Locate every malaria parasite.
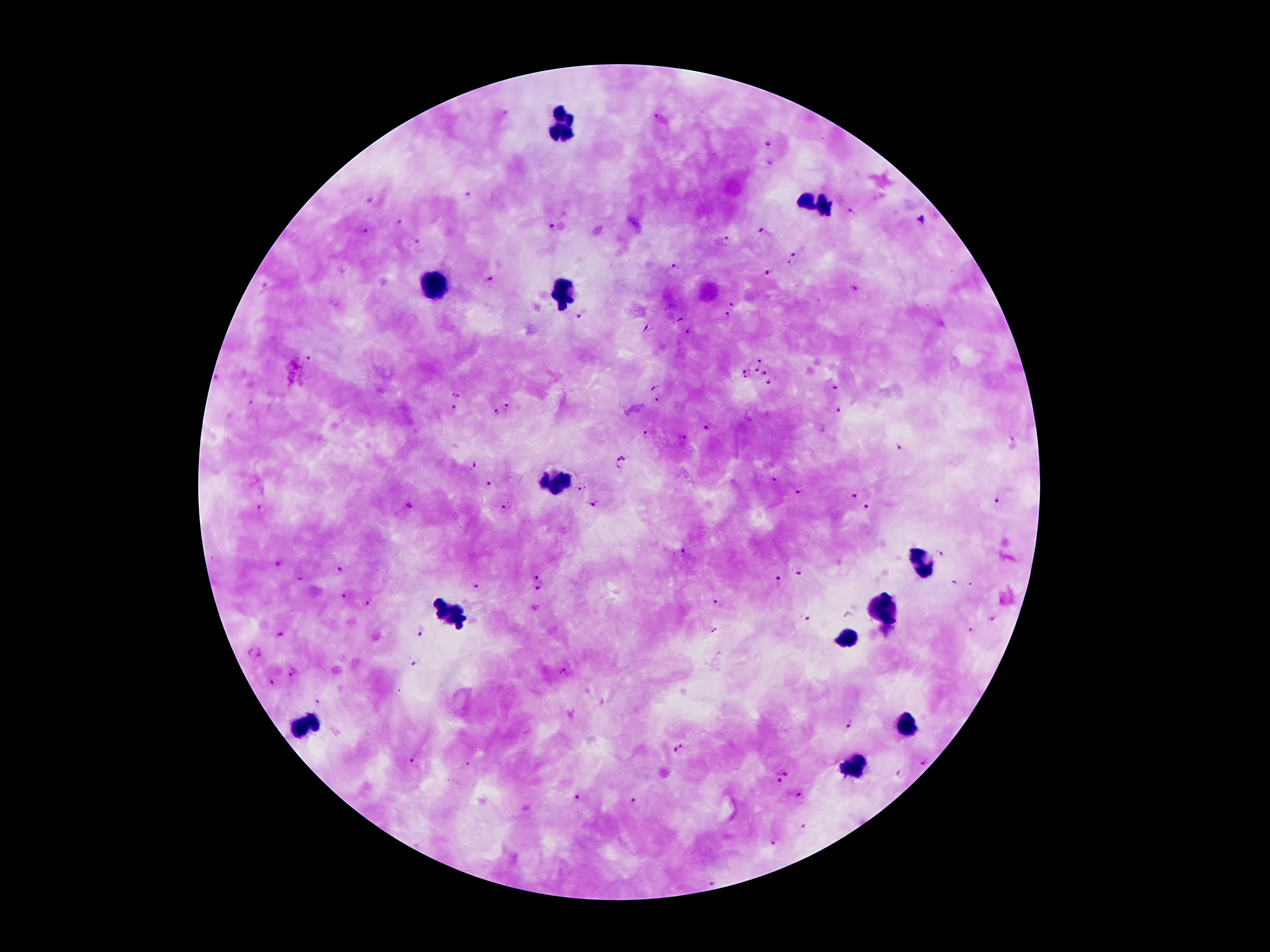
Approximate centers as [x, y] in pixels.
Malaria parasites: [657, 116], [767, 143], [771, 164], [470, 195], [851, 210], [400, 220], [552, 226], [761, 231], [366, 232], [726, 239], [415, 242], [792, 258], [674, 268], [768, 273], [491, 280], [733, 304], [578, 316], [726, 317], [679, 319], [648, 328], [685, 331], [309, 360], [757, 371], [216, 378], [654, 386], [834, 387], [455, 394], [657, 399], [252, 402], [508, 404], [454, 408], [841, 410], [496, 412], [708, 429], [645, 434], [684, 438], [1011, 440], [897, 447], [622, 462], [472, 466], [773, 480], [490, 484], [580, 488], [799, 490], [854, 494], [997, 498], [593, 504], [410, 506], [502, 506], [262, 507], [867, 509], [684, 553], [940, 554], [276, 563], [338, 569], [798, 574], [536, 576], [778, 578], [479, 585], [954, 585], [538, 588], [344, 595], [717, 601], [371, 602], [809, 619], [991, 619], [712, 631], [421, 632], [968, 633], [282, 634], [254, 653], [416, 663], [562, 672], [293, 673], [272, 682], [316, 702], [847, 724], [677, 747], [412, 763], [783, 770], [899, 773], [844, 779], [778, 780], [574, 798], [801, 799], [634, 802], [803, 829], [769, 845], [712, 883].

Leukocyte locations: [561, 127], [816, 204], [434, 278], [564, 291], [557, 480], [923, 559], [887, 607], [453, 614], [847, 638], [307, 723], [909, 727], [852, 766]. 100x magnification. Patient malaria status: positive for Plasmodium falciparum. Thick peripheral-blood smear. Giemsa-stained preparation. Photographed through the microscope eyepiece with a smartphone camera. Single field of view. Image is 1270×952 pixels.